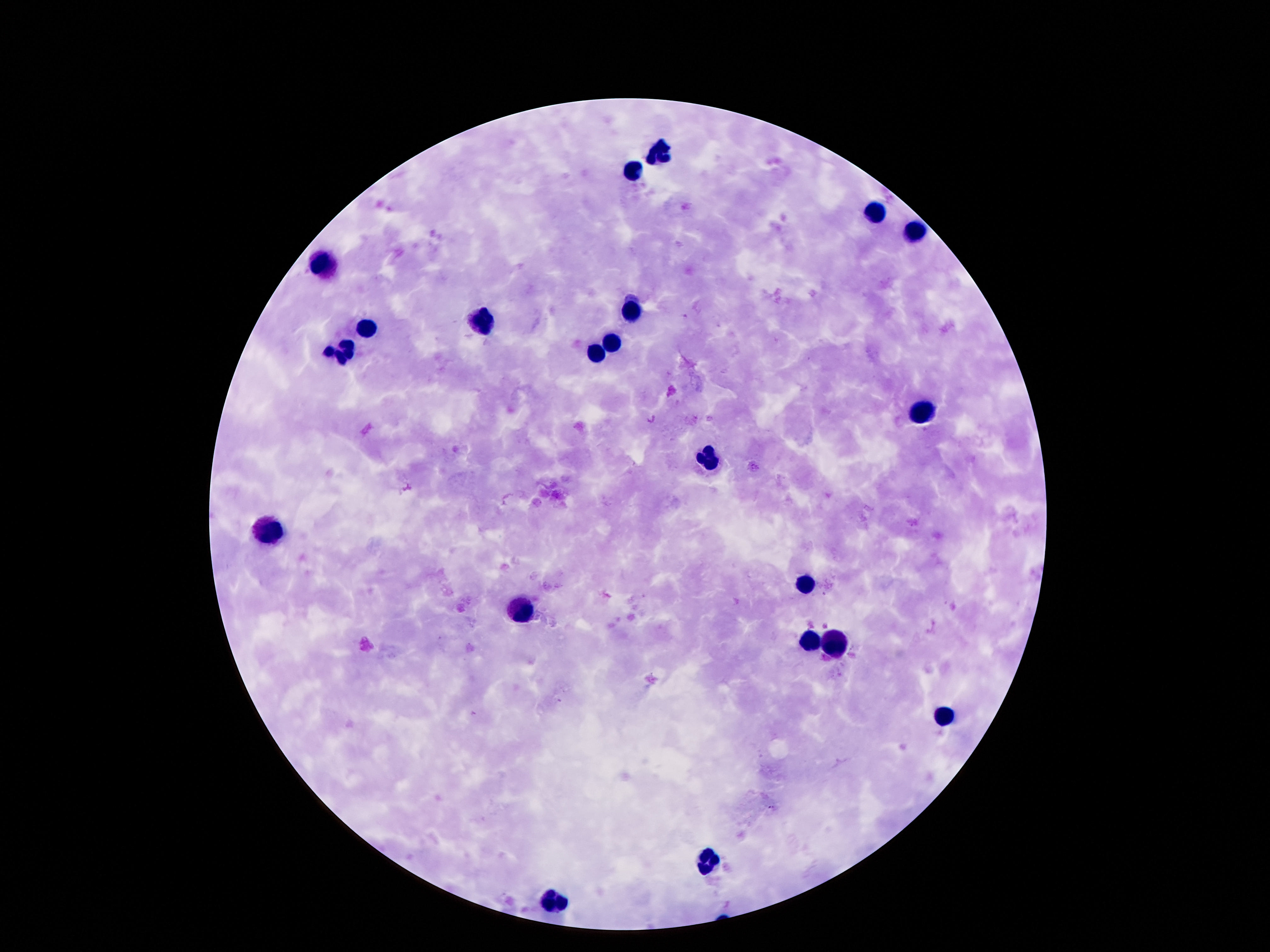

patient_malaria_status: uninfected
magnification: 100x
stain: Giemsa
field_of_view: single
capture: smartphone camera through the microscope eyepiece
image_size: 1270×952 pixels
preparation: thick peripheral-blood smear
leukocyte_locations: 'approximate centers as [x, y] in pixels: [658, 151], [634, 171], [875, 216], [915, 234], [324, 265], [632, 307], [481, 321], [364, 329], [609, 344], [597, 353], [341, 354], [921, 412], [711, 461], [268, 531], [803, 587], [520, 612], [810, 644], [833, 645], [943, 716], [711, 858], [557, 902]'